Mark where platelets are.
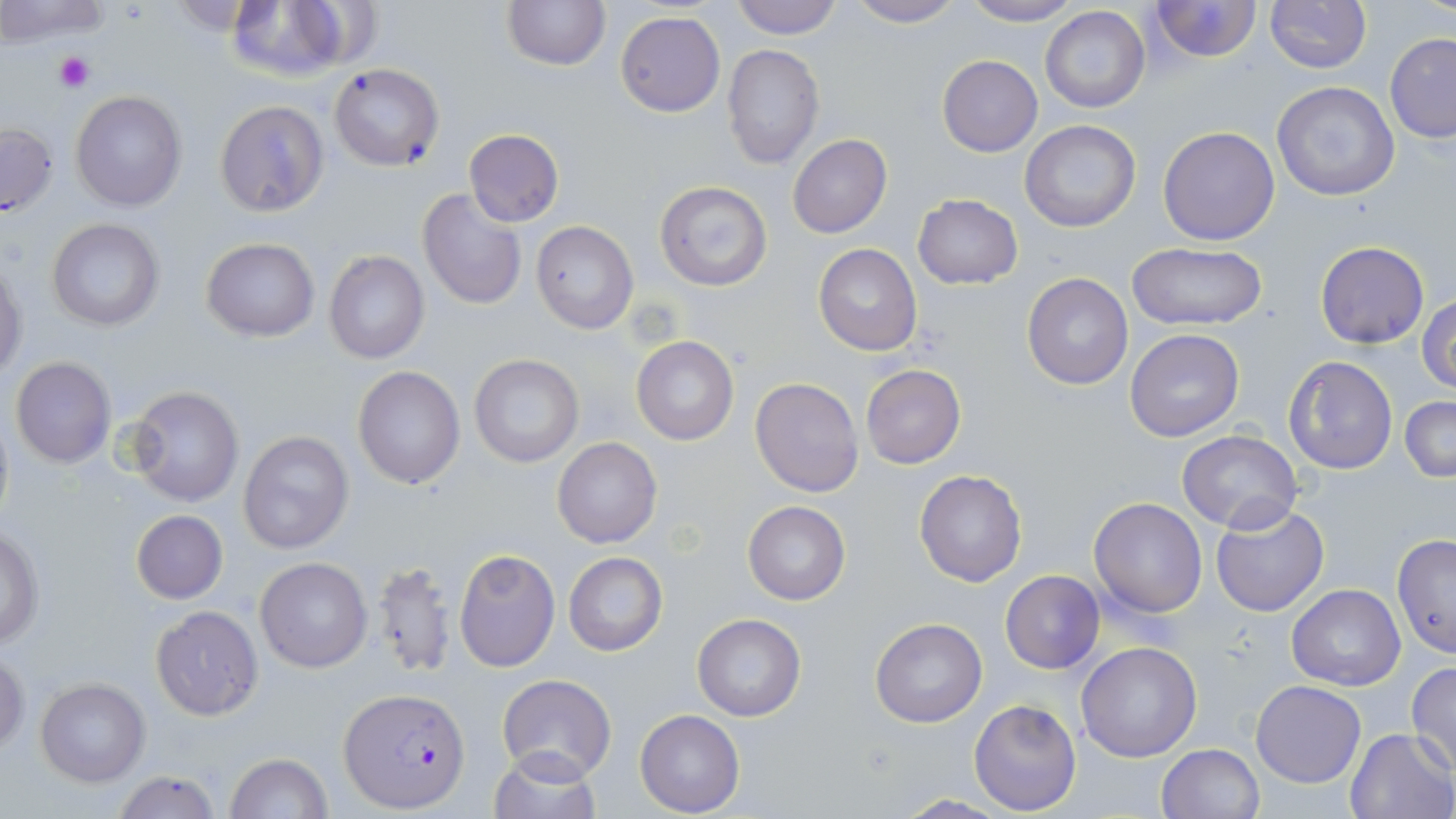

Approximate bounding boxes as (x1, y1, x2, y2) in pixels.
Platelets: (54, 51, 94, 94).

slide-level diagnosis = Plasmodium falciparum
image size = 1456×819 pixels
stain = May-Grünwald-Giemsa
uninfected red blood cell locations = approximate bounding boxes as (x1, y1, x2, y2) in pixels: (0, 0, 115, 47), (500, 0, 612, 73), (731, 0, 842, 39), (842, 0, 966, 27), (1150, 0, 1261, 64), (1265, 0, 1370, 73), (962, 1, 1080, 25), (225, 2, 358, 83), (1040, 6, 1151, 113), (616, 11, 726, 117), (1384, 32, 1456, 143), (722, 43, 824, 169), (937, 55, 1041, 156), (328, 63, 445, 171), (1270, 81, 1401, 202), (70, 90, 188, 211), (215, 100, 330, 217), (1020, 120, 1142, 233), (1, 121, 59, 219), (1157, 126, 1280, 246), (464, 129, 564, 227), (788, 135, 892, 238), (654, 180, 774, 292), (418, 188, 528, 312), (912, 194, 1022, 290), (46, 218, 165, 333), (531, 220, 639, 335), (201, 237, 321, 342), (1315, 242, 1429, 349), (813, 243, 922, 357), (1125, 243, 1269, 332), (323, 249, 430, 364), (1, 260, 26, 379), (1022, 273, 1134, 391), (1417, 293, 1456, 393), (1125, 329, 1244, 442), (631, 336, 740, 446), (469, 354, 585, 467), (1282, 354, 1399, 476), (10, 356, 117, 470), (860, 364, 966, 469), (352, 366, 466, 488), (750, 376, 865, 499), (125, 385, 245, 507), (1399, 396, 1456, 482), (0, 404, 16, 532), (238, 430, 354, 555), (1177, 430, 1302, 533), (552, 436, 662, 549), (913, 469, 1027, 587), (1089, 497, 1207, 617), (743, 501, 850, 604), (1210, 503, 1329, 617), (130, 510, 228, 604), (1, 527, 45, 648), (1392, 532, 1456, 658), (454, 549, 560, 672), (564, 551, 668, 657), (255, 557, 373, 673), (367, 557, 458, 679), (1000, 570, 1106, 674), (1286, 585, 1405, 690), (150, 606, 263, 720), (692, 613, 806, 721), (870, 617, 987, 728), (1076, 642, 1202, 763), (1, 646, 27, 756), (1406, 662, 1456, 773), (495, 674, 616, 784), (36, 679, 150, 786), (1250, 680, 1365, 787), (969, 699, 1082, 815), (634, 710, 745, 816), (1345, 728, 1456, 818), (1156, 743, 1265, 819), (485, 746, 602, 819), (224, 752, 332, 819), (109, 772, 223, 818), (892, 794, 1012, 817)
preparation = thin blood smear
magnification = 1000x
field of view = single
Plasmodium falciparum-infected red blood cell locations = approximate bounding boxes as (x1, y1, x2, y2) in pixels: (341, 687, 472, 813)
modality = light microscopy